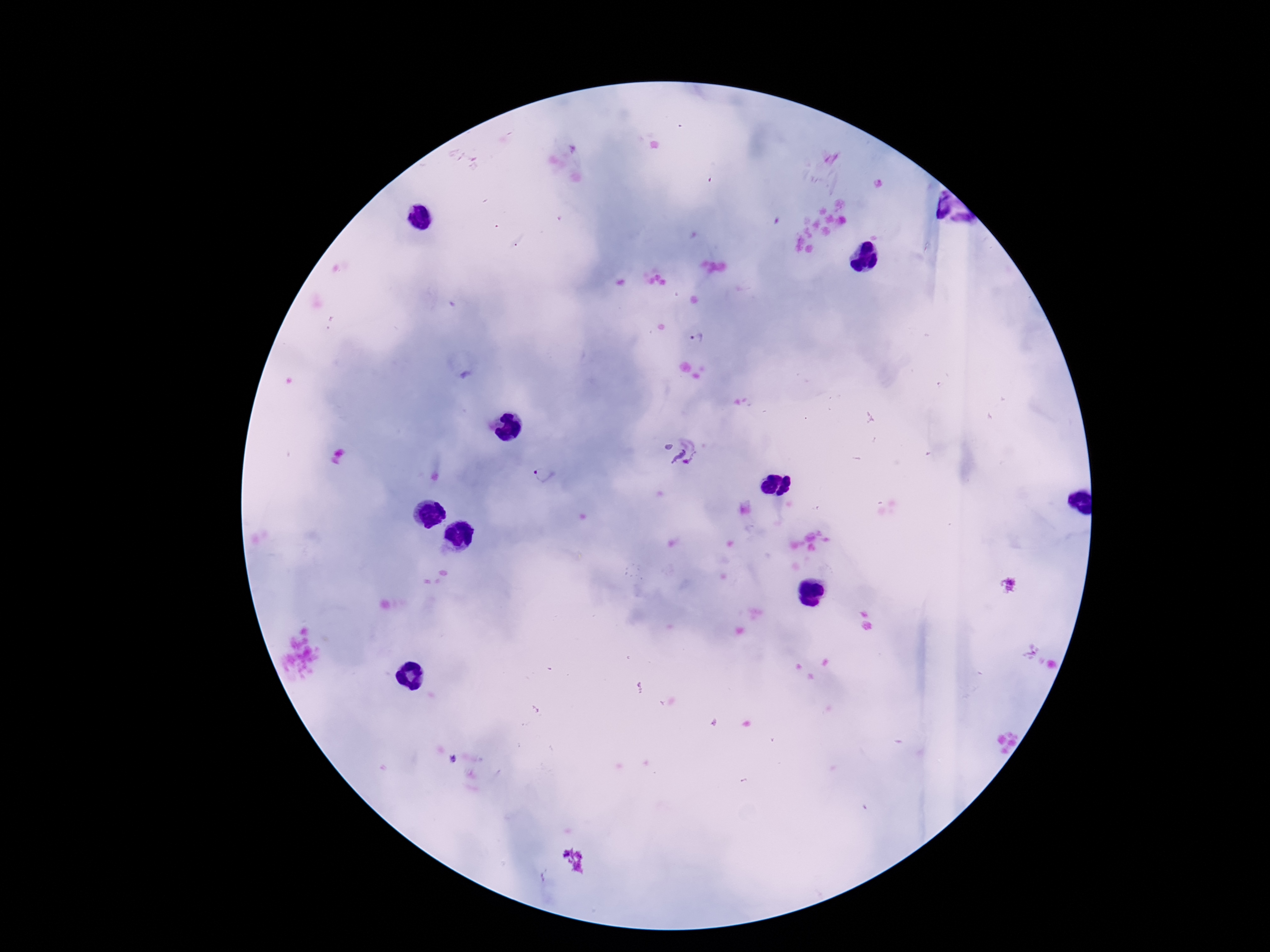
field of view = single
patient malaria status = positive
preparation = thick peripheral-blood smear
image size = 1270×952 pixels
Plasmodium parasite locations = approximate centers as {x, y} in pixels: {697, 338}, {684, 458}, {543, 476}
stain = Giemsa
capture = smartphone camera through the microscope eyepiece
magnification = 100x